Outline each blood parasite and name the species.
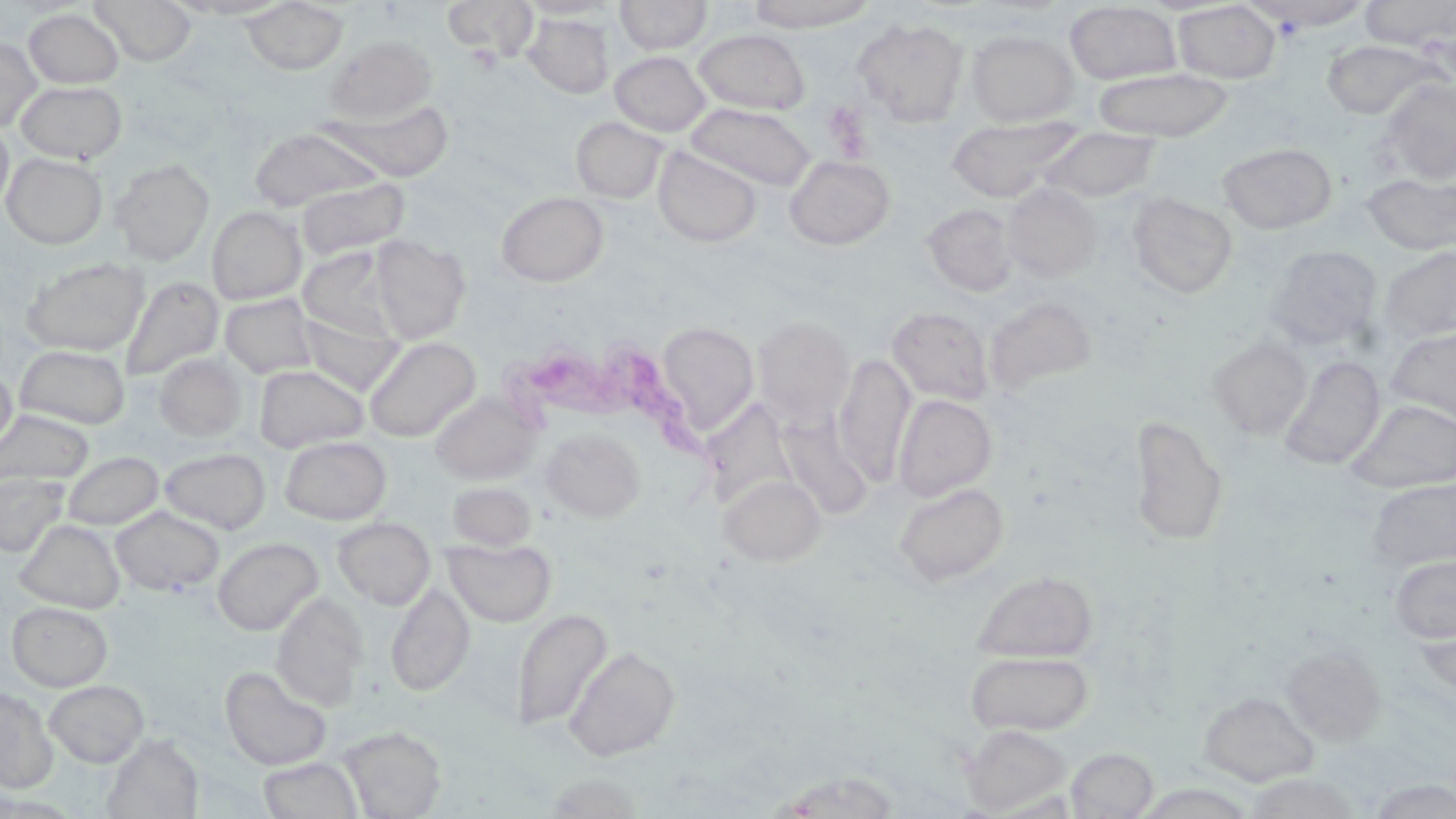
Approximate bounding boxes as [x1, y1, x2, y2] in pixels.
Trypanosoma brucei: [499, 341, 737, 490].
No Plasmodium falciparum, Plasmodium ovale, Plasmodium malariae, Plasmodium vivax, or Babesia divergens observed.

Summary:
  - Uninfected red blood cell locations: [89, 0, 197, 66], [170, 0, 295, 20], [442, 0, 538, 62], [517, 0, 619, 19], [615, 0, 712, 54], [746, 0, 876, 32], [1359, 0, 1456, 50], [241, 1, 349, 76], [1251, 1, 1374, 31], [1065, 2, 1182, 84], [1173, 2, 1281, 84], [24, 8, 124, 89], [522, 13, 614, 98], [852, 17, 969, 127], [693, 29, 810, 115], [966, 29, 1079, 126], [325, 34, 437, 122], [0, 38, 42, 133], [1321, 39, 1441, 119], [610, 51, 711, 136], [1092, 67, 1234, 141], [1378, 78, 1456, 185], [16, 80, 127, 163], [322, 97, 455, 182], [685, 102, 817, 191], [946, 115, 1084, 202], [571, 116, 669, 203], [0, 121, 14, 213], [248, 127, 385, 211], [1040, 127, 1161, 203], [1218, 142, 1337, 233], [653, 146, 761, 247], [2, 153, 107, 249], [784, 155, 895, 250], [111, 160, 214, 264], [1362, 173, 1456, 255], [296, 177, 410, 260], [1002, 183, 1102, 281], [496, 191, 609, 286], [1127, 192, 1238, 299], [922, 203, 1019, 296], [207, 206, 306, 305], [369, 236, 470, 343], [1266, 245, 1383, 350], [1378, 246, 1456, 345], [298, 247, 406, 343], [21, 256, 149, 355], [120, 275, 224, 382], [219, 293, 319, 380], [983, 296, 1098, 396], [887, 306, 994, 406], [297, 311, 404, 395], [752, 315, 855, 426], [656, 322, 759, 437], [1386, 328, 1456, 428], [363, 336, 480, 442], [1208, 336, 1312, 440], [15, 345, 130, 429], [155, 354, 246, 441], [160, 354, 254, 535], [833, 354, 916, 484], [1280, 355, 1385, 471], [254, 364, 369, 452], [0, 365, 16, 452], [432, 392, 541, 486], [893, 394, 997, 502], [701, 399, 798, 511], [1348, 399, 1456, 493], [0, 410, 92, 485], [779, 412, 873, 520], [1127, 413, 1229, 547], [542, 427, 644, 522], [281, 436, 391, 524], [159, 447, 271, 534], [62, 452, 164, 530], [0, 472, 69, 556], [719, 474, 824, 566], [1366, 477, 1456, 572], [894, 481, 1010, 587], [447, 482, 537, 551], [111, 506, 224, 596], [333, 517, 436, 609], [15, 519, 125, 613], [212, 537, 323, 635], [445, 537, 557, 627], [1389, 555, 1456, 644], [971, 569, 1099, 663], [386, 583, 475, 697], [271, 593, 368, 709], [7, 602, 112, 691], [511, 608, 612, 731], [1280, 644, 1387, 746], [565, 645, 681, 761], [965, 649, 1092, 736], [219, 665, 333, 770], [44, 680, 149, 767], [0, 686, 57, 793], [1199, 690, 1319, 786], [960, 724, 1070, 815], [338, 727, 445, 817], [103, 736, 204, 818], [1067, 748, 1159, 817], [257, 756, 364, 818], [542, 772, 645, 817], [772, 772, 902, 817], [1242, 772, 1363, 818], [1365, 777, 1456, 818]
  - Platelet locations: [823, 100, 872, 159]
  - Slide-level diagnosis: Trypanosoma brucei
  - Magnification: 1000x
  - Field of view: one of a larger specimen
  - Image size: 1456×819 pixels
  - Stain: May-Grünwald-Giemsa
  - Preparation: thin blood film
  - Modality: optical microscopy